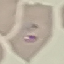 Result: malaria parasites detected. Thin blood smear. Giemsa stain. Automatically extracted cell patch, resized to 64 × 64 pixels. Photographed with a smartphone camera at the microscope eyepiece.